Classify this cell by malaria status.
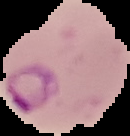

It is parasitized.

image type = segmented cell region on a black background
image size = 130×136 pixels
preparation = thin blood smear